Give the preparation type.
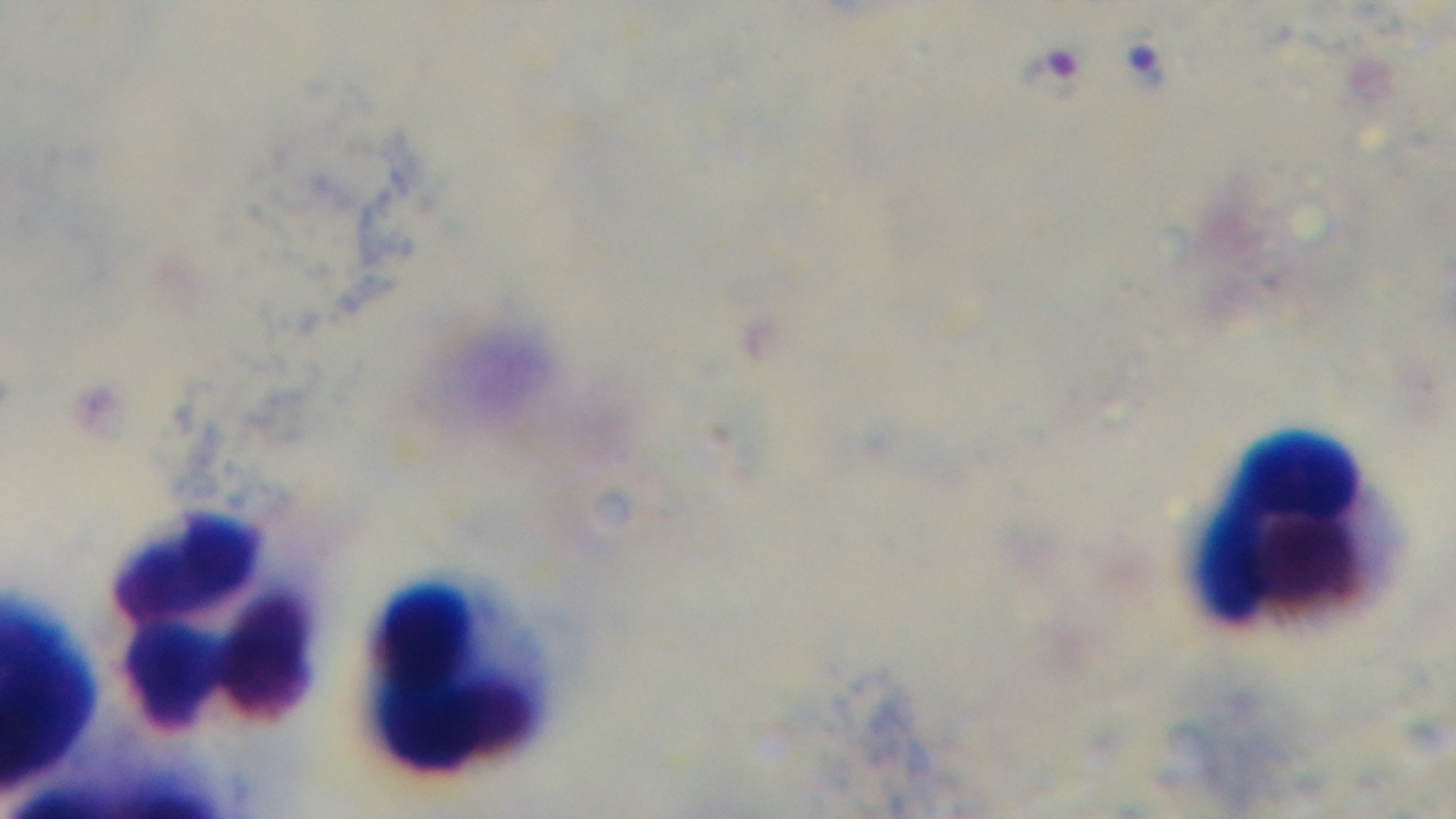
Thick.

malaria status = infected
objective = 100x oil immersion
field of view = one from the slide
capture = mounted 4K digital camera
modality = light microscopy
stain = Giemsa